State which parasite is depicted.
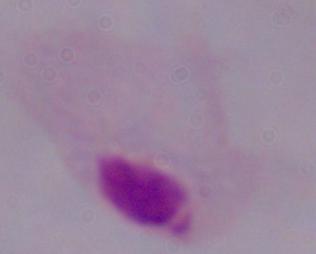

A trichomonad.

Micrograph. 1000x magnification.